Identify the cell.
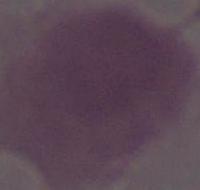

An erythrocyte.

Micrograph. Captured at 1000x magnification.